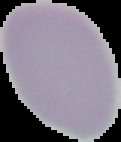 Image is 121×142 pixels. Result: no Plasmodium parasites detected. Segmented cell region on a black background. From a thin blood film.